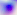
Summary:
  - Identification: Toxoplasma gondii
  - Magnification: 400x
  - Modality: micrograph